Identify the parasite.
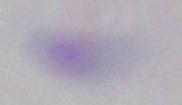

This is Toxoplasma gondii.

{
  "modality": "photomicrograph",
  "magnification": "1000x"
}